Point out each leukocyte.
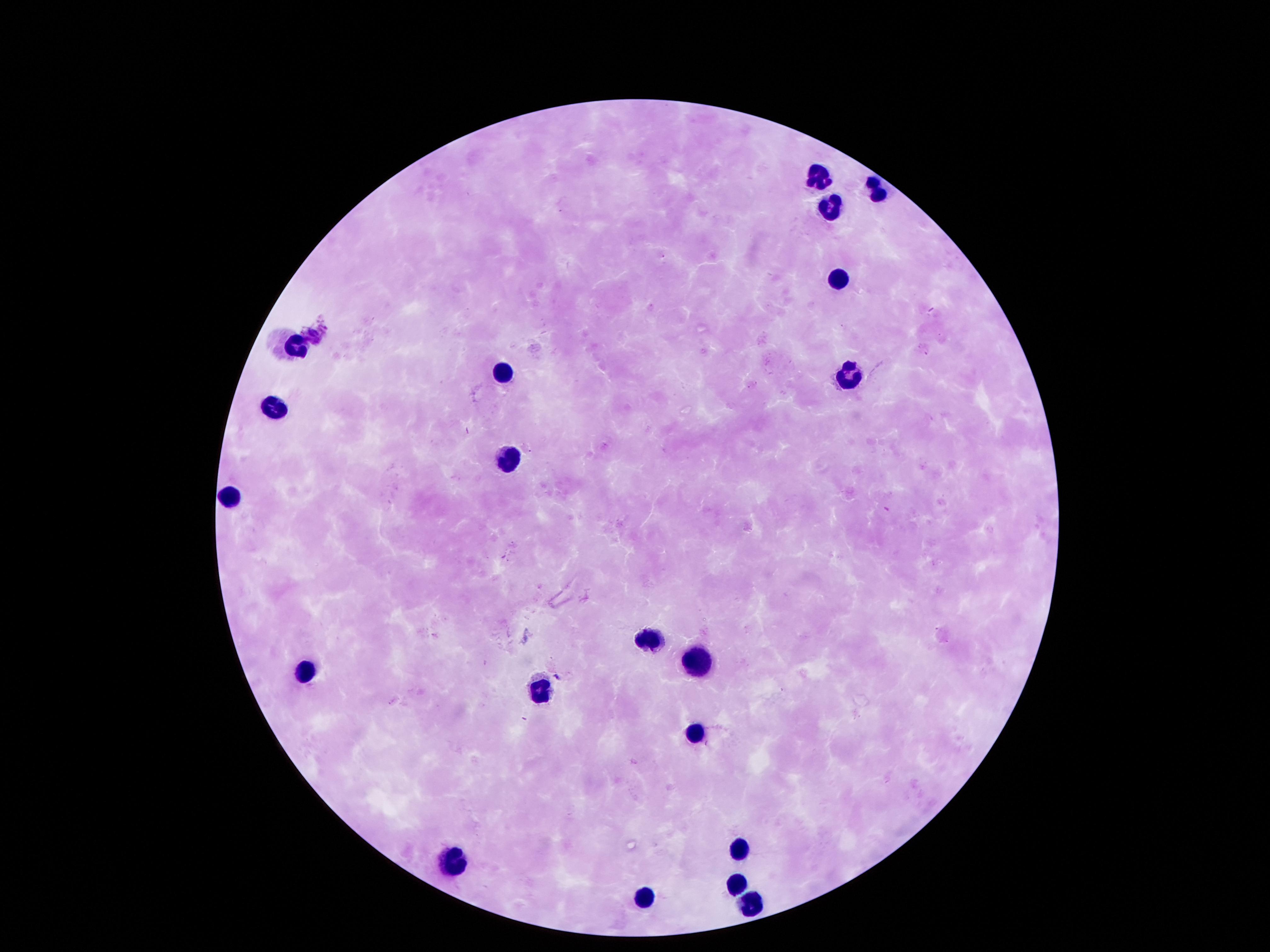
Approximate centers as [x, y] in pixels.
Leukocytes: [817, 178], [877, 185], [827, 205], [840, 282], [292, 336], [501, 370], [851, 373], [276, 405], [511, 457], [229, 494], [652, 635], [696, 659], [306, 672], [541, 689], [693, 732], [740, 847], [447, 862], [736, 880], [642, 900], [750, 900].

field of view = single
capture = smartphone camera through the microscope eyepiece
image size = 1270×952 pixels
preparation = thick blood film
stain = Giemsa
patient malaria status = negative
magnification = 100x